Classify this cell by malaria status.
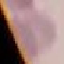
It is uninfected.

Summary:
  - Stain: Giemsa
  - Preparation: thin blood smear
  - Capture: smartphone camera at the microscope eyepiece
  - Image type: automatically extracted cell patch, resized to 64 × 64 pixels